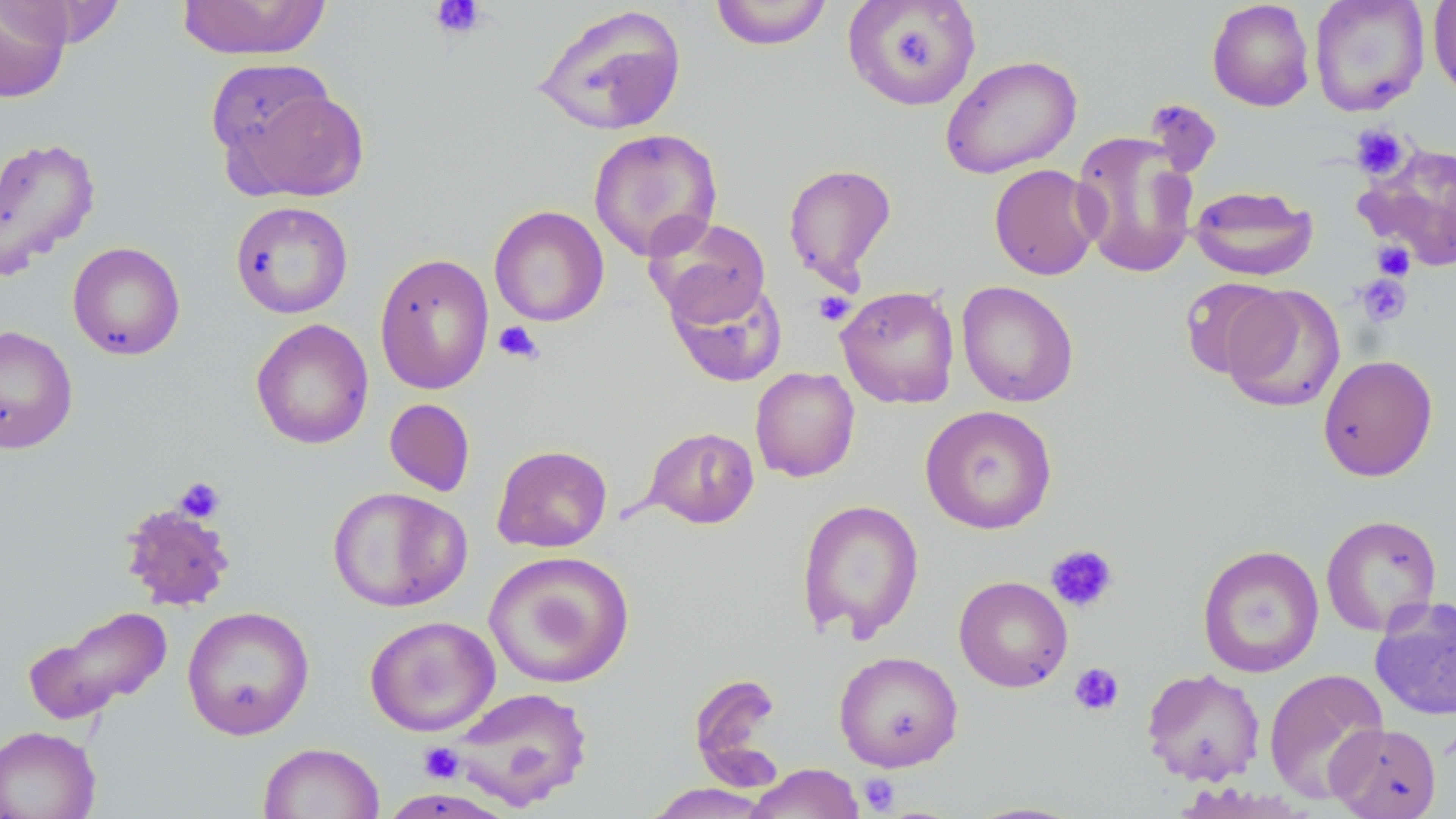

slide-level diagnosis = no evidence of blood parasites
stain = May-Grünwald-Giemsa
uninfected red blood cell locations = approximate bounding boxes as named x1/y1/x2/y2 corners in pixels: (x1=176, y1=0, x2=332, y2=61), (x1=842, y1=0, x2=982, y2=110), (x1=1206, y1=0, x2=1315, y2=112), (x1=1309, y1=0, x2=1430, y2=117), (x1=1428, y1=0, x2=1456, y2=102), (x1=0, y1=1, x2=73, y2=103), (x1=13, y1=1, x2=128, y2=47), (x1=708, y1=1, x2=834, y2=51), (x1=531, y1=4, x2=689, y2=137), (x1=939, y1=54, x2=1082, y2=179), (x1=219, y1=77, x2=368, y2=200), (x1=1144, y1=99, x2=1223, y2=178), (x1=588, y1=128, x2=723, y2=262), (x1=1071, y1=130, x2=1200, y2=279), (x1=0, y1=135, x2=101, y2=280), (x1=1357, y1=140, x2=1456, y2=272), (x1=782, y1=163, x2=898, y2=291), (x1=988, y1=163, x2=1103, y2=281), (x1=1189, y1=184, x2=1318, y2=281), (x1=230, y1=200, x2=354, y2=319), (x1=489, y1=205, x2=609, y2=327), (x1=646, y1=216, x2=771, y2=328), (x1=67, y1=242, x2=186, y2=361), (x1=374, y1=252, x2=494, y2=395), (x1=666, y1=275, x2=788, y2=387), (x1=1179, y1=277, x2=1288, y2=380), (x1=956, y1=281, x2=1079, y2=407), (x1=1221, y1=284, x2=1345, y2=413), (x1=836, y1=285, x2=960, y2=409), (x1=250, y1=318, x2=374, y2=450), (x1=0, y1=325, x2=78, y2=453), (x1=1317, y1=354, x2=1438, y2=482), (x1=750, y1=367, x2=860, y2=482), (x1=384, y1=398, x2=475, y2=496), (x1=920, y1=405, x2=1057, y2=534), (x1=642, y1=426, x2=759, y2=529), (x1=491, y1=444, x2=612, y2=553), (x1=327, y1=486, x2=471, y2=612), (x1=797, y1=498, x2=924, y2=642), (x1=118, y1=501, x2=237, y2=612), (x1=1321, y1=514, x2=1442, y2=636), (x1=1197, y1=544, x2=1325, y2=678), (x1=483, y1=551, x2=635, y2=689), (x1=953, y1=575, x2=1073, y2=692), (x1=1369, y1=597, x2=1456, y2=721), (x1=23, y1=604, x2=174, y2=726), (x1=181, y1=605, x2=315, y2=740), (x1=364, y1=615, x2=501, y2=736), (x1=833, y1=650, x2=964, y2=772), (x1=1141, y1=667, x2=1266, y2=785), (x1=1264, y1=668, x2=1390, y2=803), (x1=444, y1=686, x2=594, y2=810), (x1=1326, y1=723, x2=1442, y2=818), (x1=0, y1=725, x2=100, y2=819), (x1=257, y1=741, x2=384, y2=819), (x1=745, y1=763, x2=866, y2=819), (x1=643, y1=783, x2=776, y2=818), (x1=961, y1=800, x2=1091, y2=818)
field of view = single
image size = 1456×819 pixels
preparation = thin blood smear
magnification = 1000x
modality = light microscopy
platelet locations = approximate bounding boxes as named x1/y1/x2/y2 corners in pixels: (x1=430, y1=0, x2=487, y2=40), (x1=883, y1=20, x2=947, y2=84), (x1=1351, y1=124, x2=1410, y2=180), (x1=1372, y1=240, x2=1415, y2=281), (x1=1355, y1=273, x2=1413, y2=327), (x1=813, y1=291, x2=855, y2=326), (x1=493, y1=321, x2=543, y2=364), (x1=173, y1=477, x2=227, y2=523), (x1=1045, y1=544, x2=1119, y2=613), (x1=1069, y1=662, x2=1125, y2=716), (x1=419, y1=742, x2=464, y2=783), (x1=858, y1=773, x2=900, y2=814)